Locate every malaria parasite.
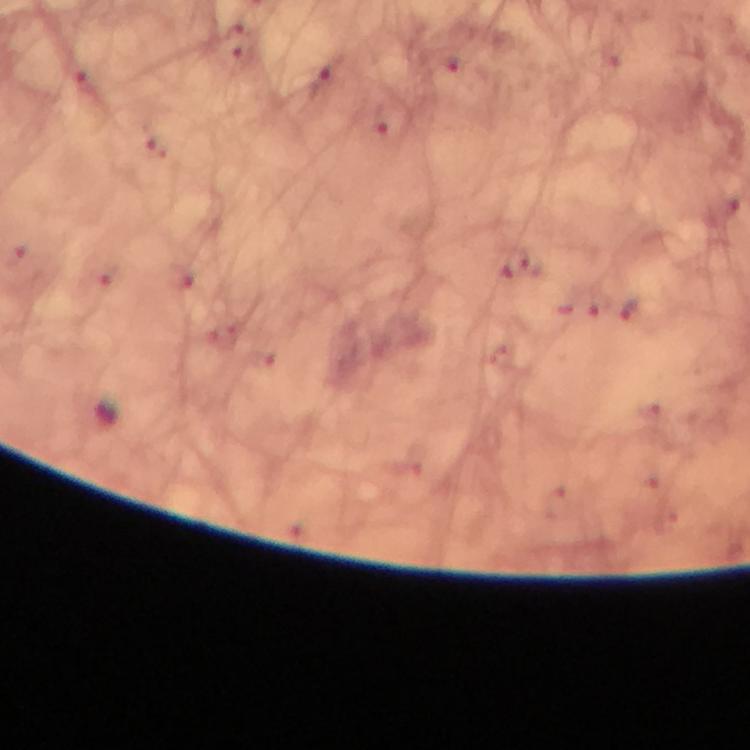
Approximate centers as (x, y) in pixels.
Malaria parasites: (320, 76), (633, 312).

Summary:
  - Context: from a malaria diagnostic workup
  - Image size: 750×750 pixels
  - Preparation: thick smear
  - Immersion oil: used
  - Stain: Giemsa
  - Magnification: 100x
  - Capture: smartphone photograph through a microscope
  - Cropped from: one field of view